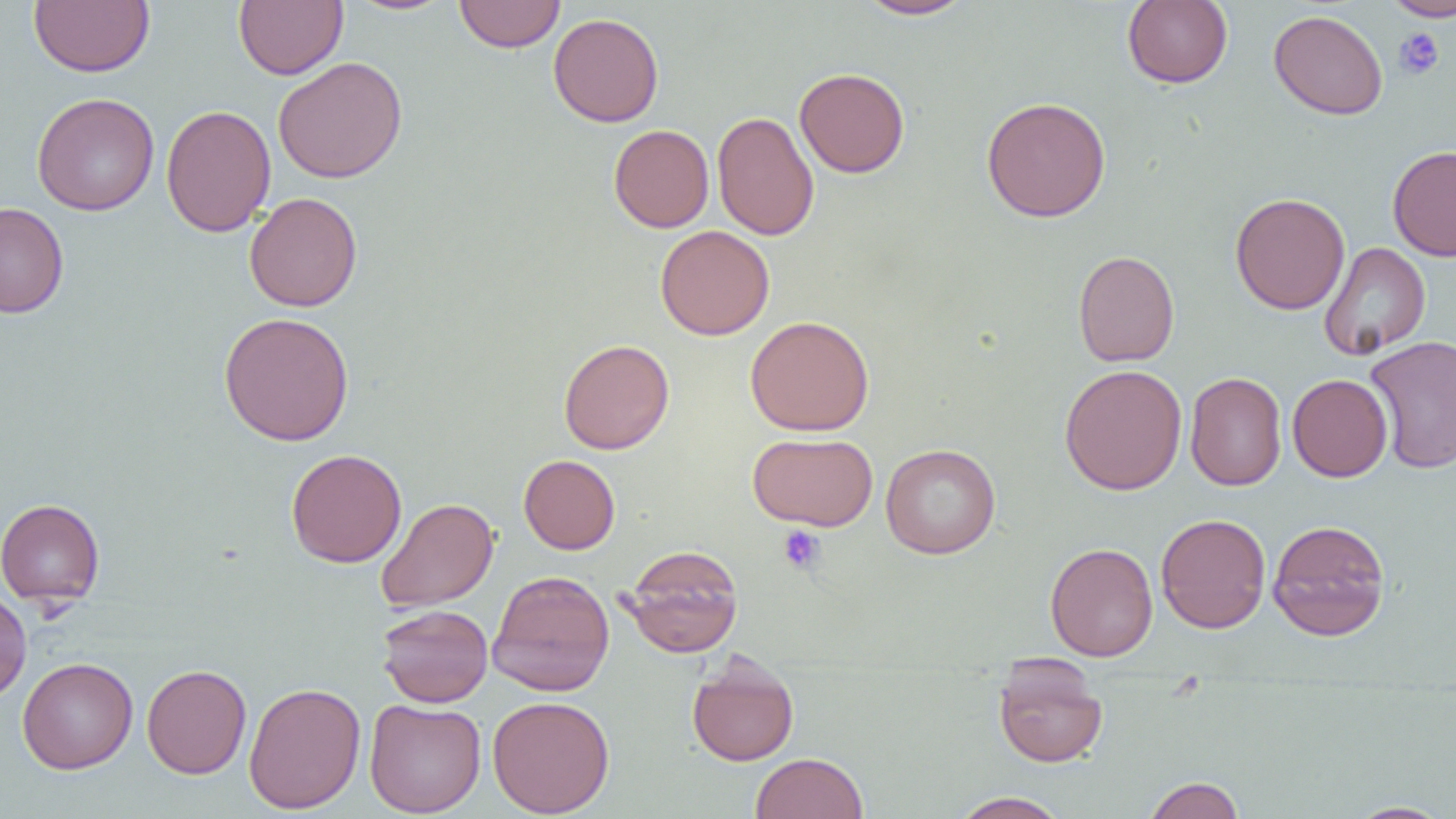

slide-level diagnosis = no evidence of blood parasites
image size = 1456×819 pixels
magnification = 1000x
field of view = one of a larger specimen
platelet locations = approximate bounding boxes as named x1/y1/x2/y2 corners in pixels: (x1=1393, y1=27, x2=1444, y2=80), (x1=777, y1=524, x2=826, y2=574)
uninfected red blood cell locations = approximate bounding boxes as named x1/y1/x2/y2 corners in pixels: (x1=28, y1=0, x2=154, y2=77), (x1=234, y1=0, x2=347, y2=80), (x1=856, y1=0, x2=975, y2=20), (x1=1121, y1=0, x2=1233, y2=89), (x1=1384, y1=0, x2=1456, y2=21), (x1=346, y1=1, x2=456, y2=16), (x1=454, y1=1, x2=565, y2=53), (x1=1268, y1=9, x2=1389, y2=120), (x1=548, y1=12, x2=664, y2=127), (x1=273, y1=56, x2=408, y2=183), (x1=794, y1=67, x2=910, y2=178), (x1=31, y1=92, x2=160, y2=216), (x1=981, y1=96, x2=1111, y2=222), (x1=160, y1=104, x2=276, y2=237), (x1=712, y1=110, x2=819, y2=241), (x1=608, y1=124, x2=714, y2=232), (x1=1387, y1=144, x2=1456, y2=261), (x1=244, y1=192, x2=362, y2=312), (x1=1230, y1=192, x2=1350, y2=315), (x1=0, y1=202, x2=69, y2=317), (x1=655, y1=225, x2=774, y2=340), (x1=1318, y1=241, x2=1431, y2=360), (x1=1073, y1=249, x2=1179, y2=367), (x1=218, y1=312, x2=355, y2=446), (x1=745, y1=315, x2=875, y2=435), (x1=1365, y1=335, x2=1456, y2=473), (x1=559, y1=338, x2=674, y2=454), (x1=1059, y1=364, x2=1187, y2=495), (x1=1185, y1=372, x2=1286, y2=491), (x1=1287, y1=374, x2=1393, y2=482), (x1=747, y1=432, x2=878, y2=531), (x1=880, y1=443, x2=1001, y2=559), (x1=285, y1=448, x2=407, y2=568), (x1=519, y1=454, x2=620, y2=554), (x1=0, y1=497, x2=105, y2=605), (x1=375, y1=498, x2=499, y2=612), (x1=1155, y1=513, x2=1271, y2=634), (x1=1266, y1=518, x2=1391, y2=641), (x1=1045, y1=542, x2=1158, y2=661), (x1=620, y1=544, x2=744, y2=658), (x1=488, y1=570, x2=615, y2=697), (x1=0, y1=588, x2=31, y2=702), (x1=376, y1=604, x2=493, y2=708), (x1=686, y1=653, x2=800, y2=766), (x1=17, y1=657, x2=138, y2=774), (x1=992, y1=660, x2=1109, y2=769), (x1=142, y1=664, x2=251, y2=779), (x1=243, y1=681, x2=366, y2=814), (x1=487, y1=695, x2=615, y2=817), (x1=363, y1=698, x2=486, y2=817), (x1=750, y1=752, x2=868, y2=819), (x1=1142, y1=776, x2=1245, y2=818), (x1=948, y1=791, x2=1072, y2=819), (x1=1344, y1=800, x2=1454, y2=818)
preparation = thin blood smear
modality = light microscopy